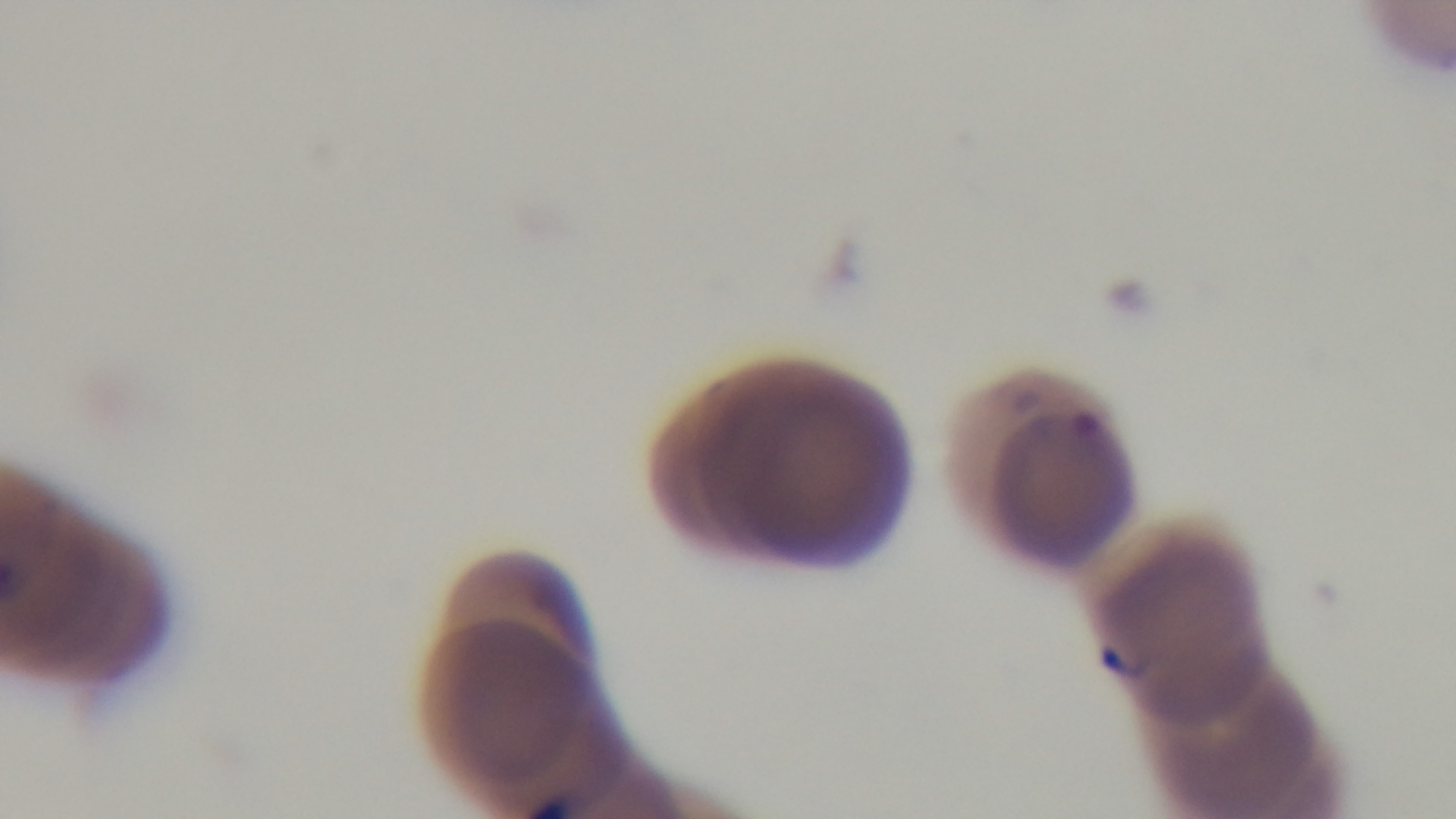
Giemsa-stained. Captured with a mounted 4K digital camera. 100x oil-immersion objective. One field from the slide. Light microscopy. Preparation: thin blood film. Malaria status: positive.